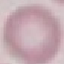
Malaria status: uninfected. Photographed with a smartphone camera at the microscope eyepiece. Automatically extracted cell patch, resized to 64 × 64 pixels. Thin smear of blood. Giemsa stain.